Report the malaria status of this cell.
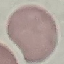
Uninfected.

stain = Giemsa
capture = smartphone camera at the microscope eyepiece
image type = cell patch, automatically extracted from a larger field of view and resized to 64 × 64 pixels
preparation = thin blood smear